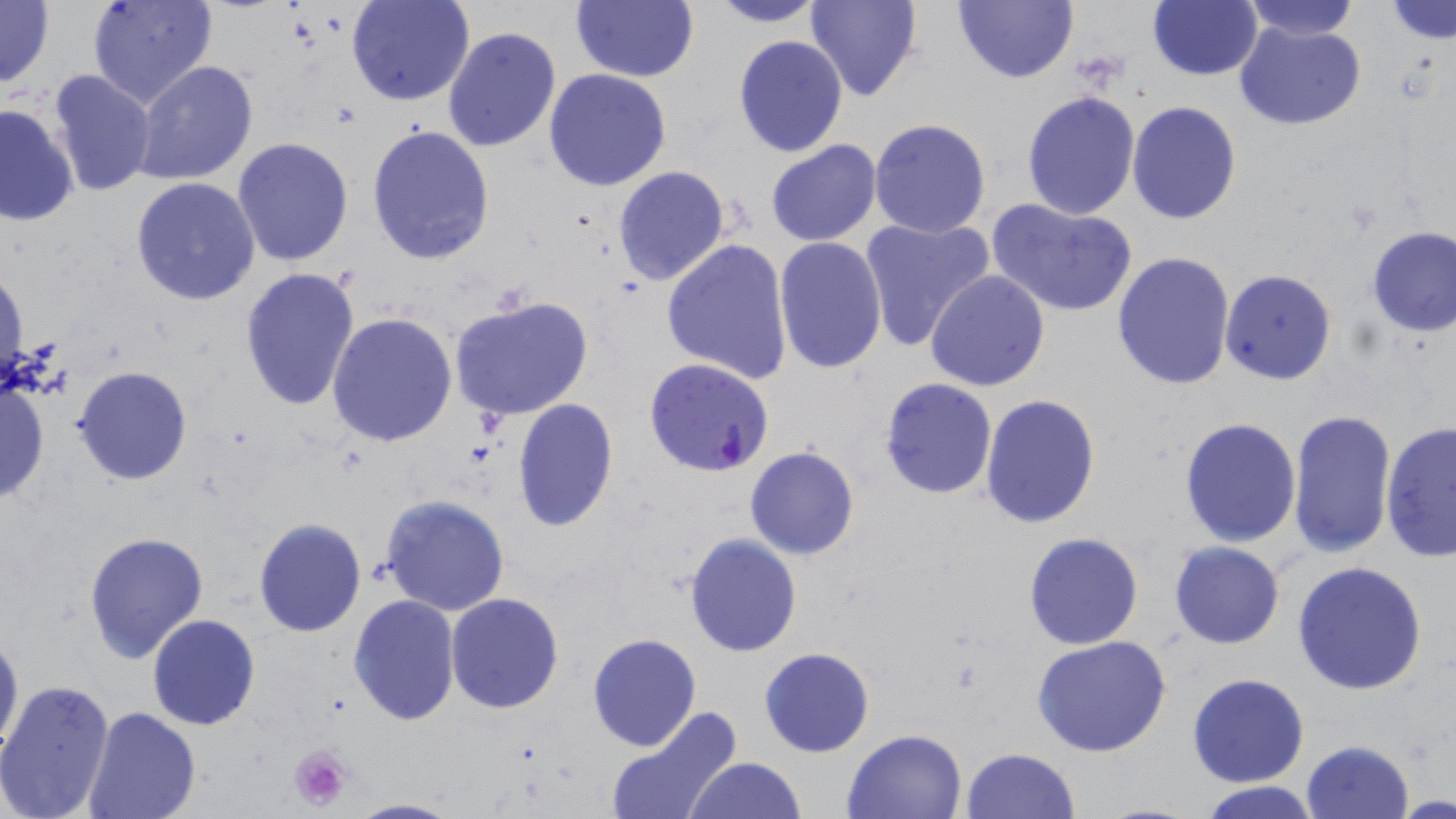

{
  "slide_level_diagnosis": "Plasmodium falciparum",
  "image_size": "1456×819 pixels",
  "plasmodium_falciparum_infected_red_blood_cell_locations": "approximate bounding boxes as [x1, y1, x2, y2] in pixels: [645, 358, 775, 477]",
  "modality": "light microscopy",
  "stain": "May-Grünwald-Giemsa",
  "preparation": "thin blood smear",
  "uninfected_red_blood_cell_locations": "approximate bounding boxes as [x1, y1, x2, y2] in pixels: [0, 0, 54, 90], [88, 0, 219, 109], [347, 0, 474, 105], [806, 0, 922, 102], [952, 0, 1077, 84], [1236, 0, 1363, 39], [570, 1, 698, 83], [708, 1, 825, 27], [1148, 1, 1263, 80], [1385, 2, 1456, 45], [1234, 20, 1367, 130], [442, 27, 559, 152], [732, 34, 849, 157], [133, 61, 260, 185], [543, 68, 671, 191], [46, 69, 156, 195], [1021, 90, 1140, 219], [1127, 100, 1243, 224], [0, 104, 79, 228], [869, 118, 993, 238], [367, 125, 495, 267], [232, 136, 355, 267], [764, 139, 883, 246], [612, 167, 730, 285], [131, 177, 260, 305], [987, 198, 1139, 318], [860, 215, 995, 349], [1365, 225, 1456, 337], [773, 237, 887, 374], [661, 238, 793, 384], [1112, 252, 1237, 393], [1, 263, 28, 391], [240, 268, 362, 414], [925, 269, 1051, 391], [1220, 269, 1337, 385], [446, 294, 596, 423], [327, 312, 459, 448], [74, 366, 192, 484], [0, 377, 50, 506], [879, 377, 997, 500], [980, 395, 1101, 528], [511, 398, 619, 532], [1286, 410, 1397, 562], [1178, 416, 1301, 548], [1379, 419, 1456, 562], [744, 445, 859, 560], [379, 493, 512, 617], [252, 518, 367, 637], [82, 530, 210, 666], [685, 532, 802, 656], [1024, 532, 1144, 650], [1169, 542, 1285, 649], [1292, 561, 1429, 695], [446, 592, 563, 714], [348, 593, 462, 726], [148, 613, 261, 730], [0, 626, 23, 762], [586, 632, 701, 751], [1031, 635, 1173, 757], [759, 646, 874, 757], [1187, 672, 1309, 787], [0, 679, 115, 819], [606, 705, 742, 819], [81, 707, 200, 819], [842, 729, 968, 819], [1300, 739, 1415, 819], [959, 748, 1080, 819], [684, 756, 804, 819], [1198, 782, 1323, 819], [345, 797, 465, 819]",
  "platelet_locations": "approximate bounding boxes as [x1, y1, x2, y2] in pixels: [1074, 55, 1125, 88], [286, 744, 353, 814]",
  "magnification": "1000x",
  "field_of_view": "single"
}